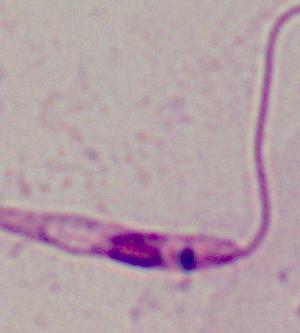 Micrograph. 1000x magnification. A Leishmania parasite is shown.